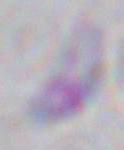
identification = Toxoplasma gondii
magnification = 1000x
modality = micrograph